Comment on the morphology of the red blood cells.
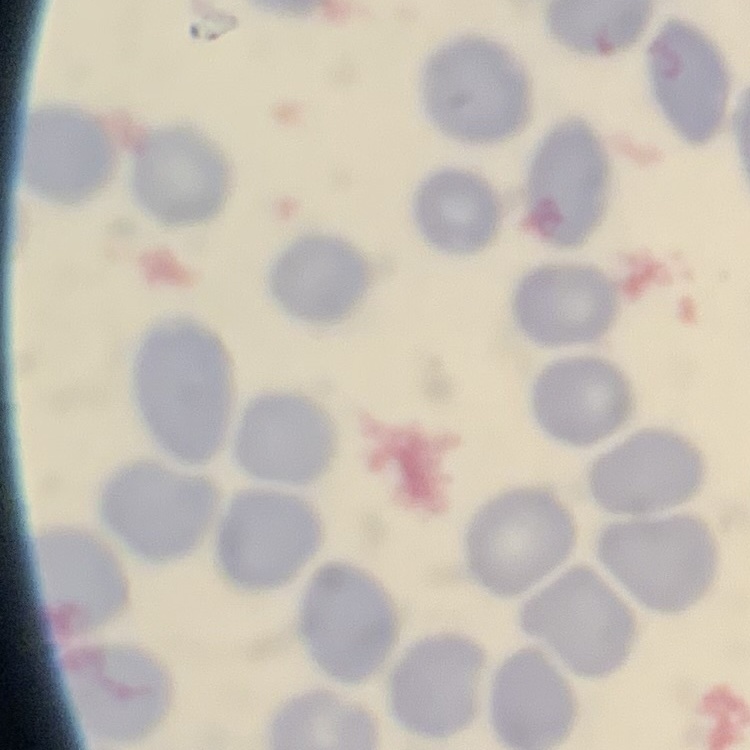

No rouleaux formation.

{
  "image_type": "one tile cut from a larger photomicrograph",
  "preparation": "thin blood film",
  "stain": "Field's or Giemsa"
}